Locate every uninfected red blood cell.
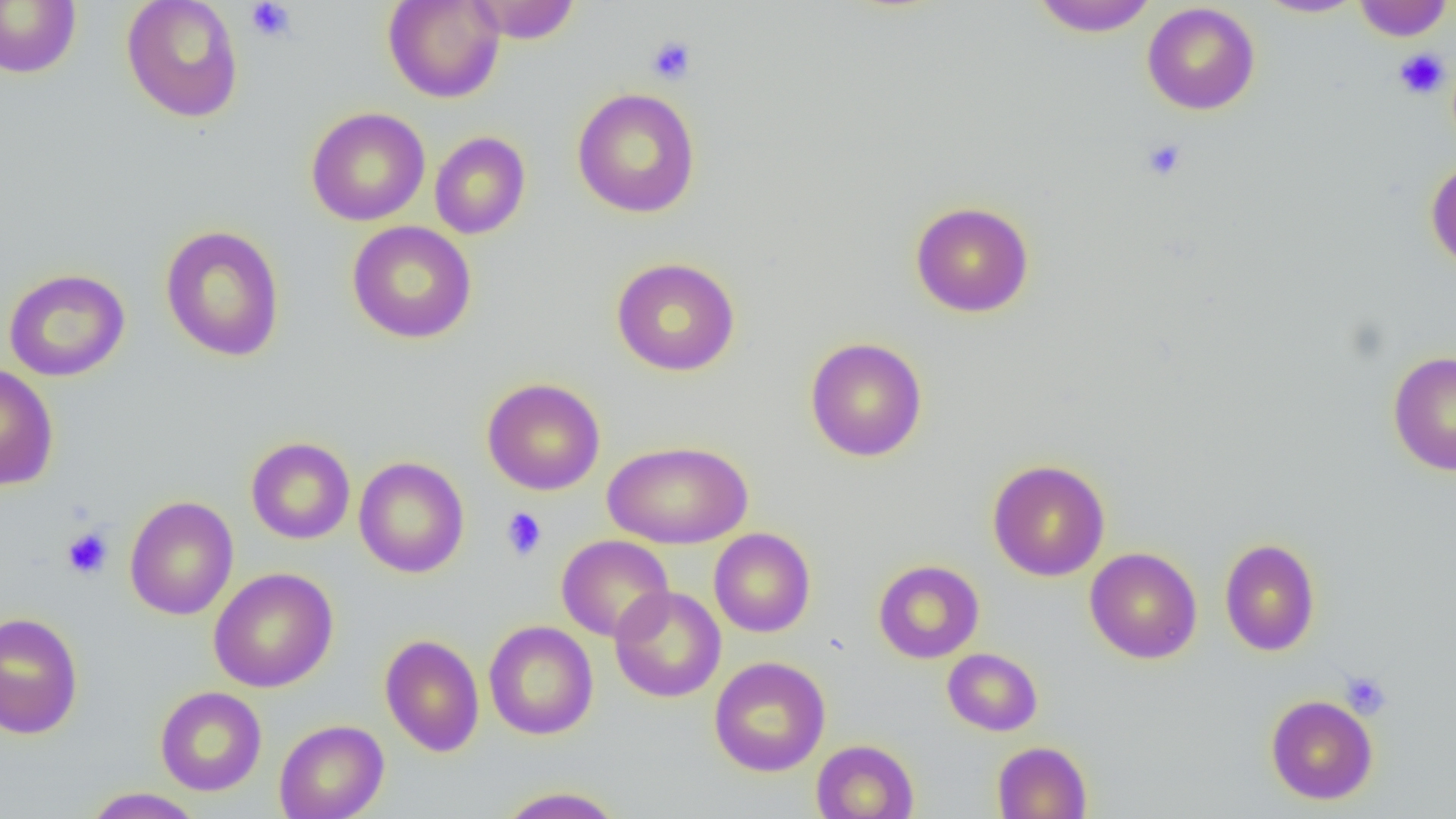

Approximate bounding boxes as (x1,y1)-(x2,y2) corner pairs in pixels.
Uninfected red blood cells: (0,0)-(81,78), (121,0)-(244,123), (382,0)-(505,104), (468,0)-(582,43), (1029,0)-(1160,37), (1253,0)-(1367,18), (1351,0)-(1453,41), (1142,2)-(1260,115), (571,87)-(701,218), (305,106)-(430,226), (429,131)-(531,239), (1426,158)-(1456,270), (910,201)-(1035,318), (347,221)-(477,343), (159,225)-(286,362), (611,257)-(741,377), (3,268)-(130,382), (805,337)-(928,462), (1388,350)-(1456,475), (0,363)-(59,490), (482,377)-(606,496), (245,437)-(356,544), (603,440)-(753,549), (353,457)-(469,578), (987,459)-(1110,581), (123,495)-(239,620), (709,528)-(816,637), (556,534)-(674,642), (1220,538)-(1320,656), (1085,547)-(1203,664), (873,559)-(984,663), (208,567)-(338,692), (610,586)-(726,702), (0,612)-(84,739), (484,621)-(599,740), (380,633)-(485,757), (942,648)-(1043,736), (709,656)-(830,777), (155,686)-(267,796), (1265,694)-(1379,805), (274,719)-(389,819), (811,739)-(919,819), (992,741)-(1092,818), (495,786)-(626,818), (81,787)-(204,818).

{
  "slide_level_diagnosis": "no evidence of blood parasites",
  "magnification": "1000x",
  "modality": "optical microscopy",
  "preparation": "thin blood film",
  "platelet_locations": "approximate bounding boxes as (x1,y1)-(x2,y2) corner pairs in pixels: (246,1)-(297,43), (646,35)-(697,85), (1393,48)-(1450,99), (1141,138)-(1187,181), (501,507)-(547,560), (62,527)-(113,580), (1340,672)-(1391,719)",
  "field_of_view": "single",
  "image_size": "1456×819 pixels"
}